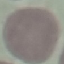
result: no malaria parasites seen
preparation: thin smear
capture: smartphone camera at the microscope eyepiece
image_type: automatically extracted cell patch, resized to 64 × 64 pixels
stain: Giemsa